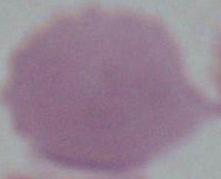

{
  "identification": "red blood cell",
  "magnification": "1000x",
  "modality": "micrograph"
}